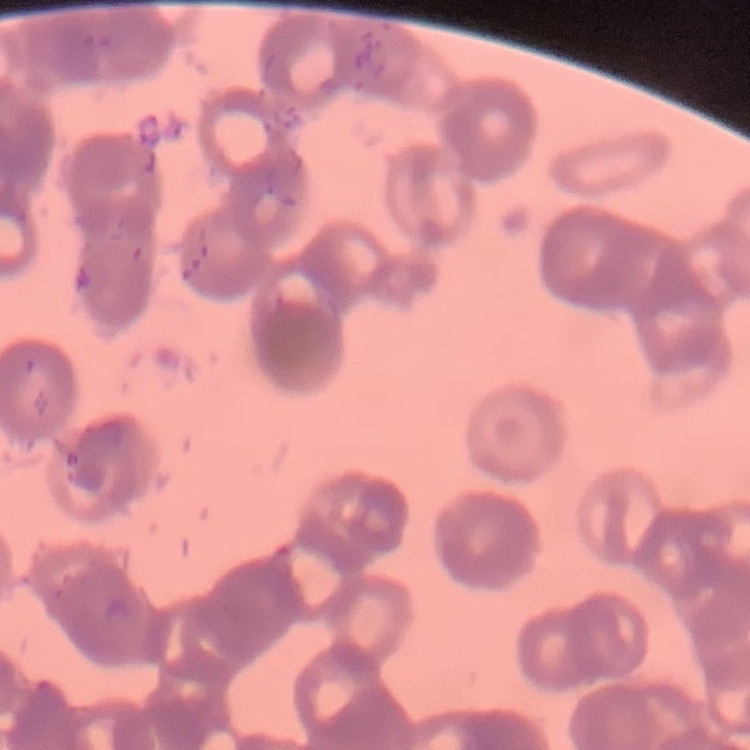

The erythrocytes show rouleaux formation. Thin blood film. Field's or Giemsa stain. One tile cut from a larger photomicrograph.